Name the cell type shown.
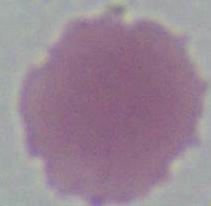
An erythrocyte.

magnification: 1000x
modality: micrograph